Locate every blood parasite and identify its species.
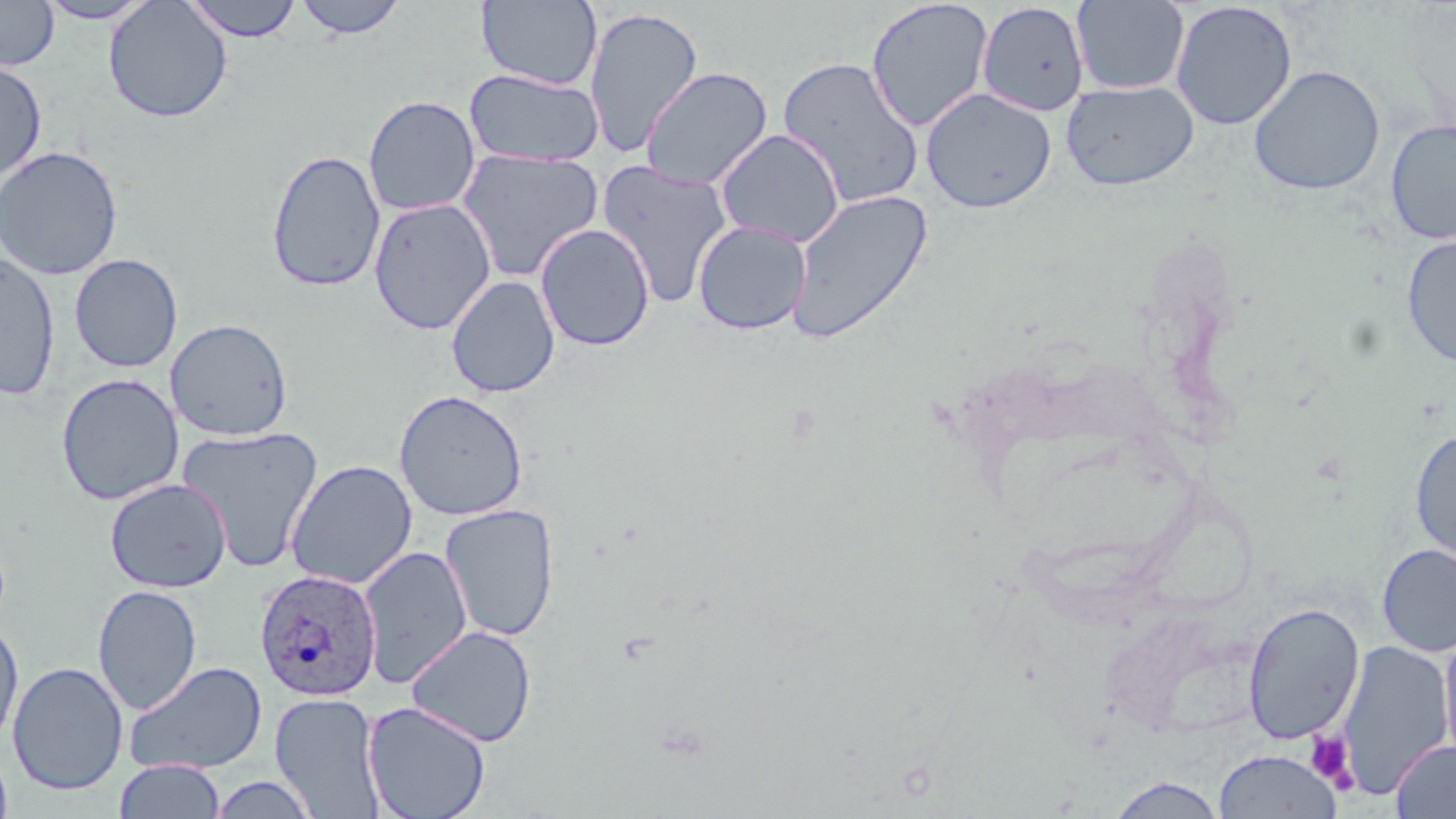
Approximate bounding boxes as named x1/y1/x2/y2 corners in pixels.
Plasmodium ovale-infected red blood cells: (x1=254, y1=568, x2=382, y2=703).
No Plasmodium falciparum, Plasmodium malariae, Plasmodium vivax, Babesia divergens, or Trypanosoma brucei observed.

Summary:
  - Platelet locations: (x1=1305, y1=731, x2=1356, y2=787)
  - Uninfected red blood cell locations: (x1=34, y1=0, x2=156, y2=24), (x1=183, y1=0, x2=303, y2=42), (x1=294, y1=0, x2=408, y2=39), (x1=476, y1=0, x2=603, y2=90), (x1=866, y1=0, x2=993, y2=133), (x1=0, y1=1, x2=60, y2=70), (x1=104, y1=1, x2=232, y2=122), (x1=1072, y1=1, x2=1190, y2=95), (x1=1170, y1=1, x2=1297, y2=131), (x1=976, y1=2, x2=1090, y2=116), (x1=583, y1=6, x2=704, y2=159), (x1=777, y1=56, x2=925, y2=209), (x1=0, y1=59, x2=47, y2=184), (x1=1249, y1=65, x2=1385, y2=196), (x1=639, y1=66, x2=773, y2=191), (x1=463, y1=68, x2=604, y2=167), (x1=1061, y1=80, x2=1199, y2=191), (x1=920, y1=87, x2=1057, y2=213), (x1=363, y1=95, x2=481, y2=217), (x1=1385, y1=118, x2=1456, y2=245), (x1=715, y1=128, x2=845, y2=248), (x1=0, y1=145, x2=123, y2=280), (x1=455, y1=148, x2=604, y2=283), (x1=266, y1=149, x2=386, y2=293), (x1=596, y1=159, x2=735, y2=309), (x1=787, y1=188, x2=933, y2=343), (x1=369, y1=197, x2=496, y2=335), (x1=693, y1=219, x2=812, y2=334), (x1=535, y1=223, x2=655, y2=351), (x1=1401, y1=236, x2=1456, y2=367), (x1=0, y1=251, x2=60, y2=400), (x1=69, y1=253, x2=183, y2=373), (x1=446, y1=275, x2=560, y2=398), (x1=166, y1=318, x2=293, y2=441), (x1=56, y1=373, x2=184, y2=505), (x1=393, y1=389, x2=529, y2=521), (x1=176, y1=426, x2=324, y2=572), (x1=1410, y1=429, x2=1456, y2=567), (x1=285, y1=460, x2=417, y2=589), (x1=105, y1=478, x2=231, y2=593), (x1=440, y1=504, x2=559, y2=642), (x1=1376, y1=543, x2=1456, y2=657), (x1=359, y1=545, x2=471, y2=688), (x1=93, y1=584, x2=203, y2=715), (x1=1242, y1=602, x2=1365, y2=745), (x1=0, y1=617, x2=24, y2=749), (x1=1438, y1=622, x2=1456, y2=772), (x1=405, y1=624, x2=537, y2=747), (x1=1336, y1=640, x2=1454, y2=800), (x1=124, y1=660, x2=267, y2=776), (x1=7, y1=661, x2=128, y2=795), (x1=270, y1=692, x2=385, y2=818), (x1=362, y1=700, x2=491, y2=819), (x1=1390, y1=740, x2=1456, y2=818), (x1=0, y1=741, x2=13, y2=819), (x1=1214, y1=749, x2=1342, y2=819), (x1=115, y1=758, x2=226, y2=818), (x1=208, y1=774, x2=319, y2=818), (x1=1106, y1=776, x2=1228, y2=818)
  - Slide-level diagnosis: Plasmodium ovale
  - Modality: optical microscopy
  - Stain: May-Grünwald-Giemsa
  - Magnification: 1000x
  - Preparation: thin blood film
  - Field of view: single
  - Image size: 1456×819 pixels